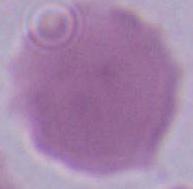
Summary:
  - Magnification: 1000x
  - Identification: red blood cell
  - Modality: micrograph